Assess this cell for malaria.
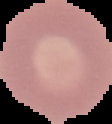

Uninfected.

From a thin blood film. Cell region segmented out of the field of view; the surrounding area is masked to black. Image is 112×124 pixels.